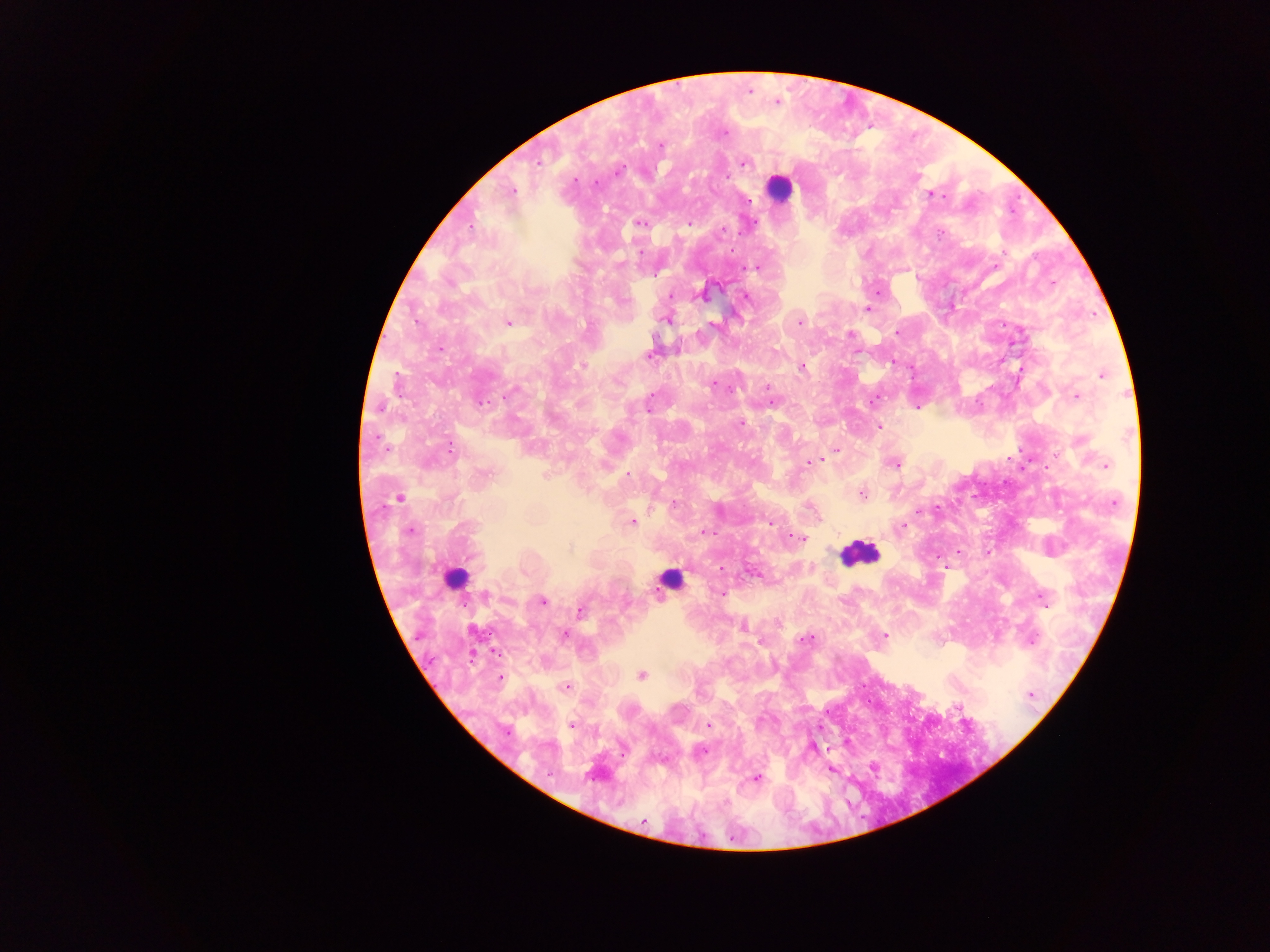

Approximate centers as (x, y) in pixels. Plasmodium parasite locations: (776, 102), (723, 133), (659, 147), (743, 161), (618, 171), (575, 181), (516, 192), (930, 197), (747, 200), (639, 222), (687, 224), (739, 234), (940, 234), (752, 267), (1052, 283), (669, 296), (746, 297), (866, 308), (799, 319), (508, 323), (896, 332), (849, 334), (441, 349), (651, 354), (892, 362), (801, 367), (398, 373), (1100, 378), (714, 383), (767, 385), (1075, 395), (398, 396), (504, 398), (649, 401), (484, 402), (868, 403), (771, 405), (917, 409), (880, 426), (451, 447), (838, 449), (1009, 458), (1030, 459), (814, 461), (807, 462), (1108, 463), (891, 465), (1045, 467), (628, 476), (861, 494), (631, 522), (769, 523), (904, 527), (409, 530), (703, 531), (715, 534), (788, 537), (802, 537), (961, 552), (722, 566), (945, 567), (723, 592), (544, 600), (580, 611), (563, 635), (883, 636), (807, 638), (499, 679), (565, 686), (871, 702), (571, 725), (708, 725), (701, 750), (756, 777), (641, 821). Leukocyte locations: (786, 192), (862, 554), (451, 576), (665, 581). Thick blood film. Image is 1270×952 pixels. One field of view. Collected in Ghana. Mobile-phone photograph taken through the microscope.